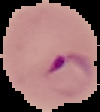
malaria status = parasitized
image type = segmented cell region on a black background
preparation = thin blood smear
image size = 100×112 pixels